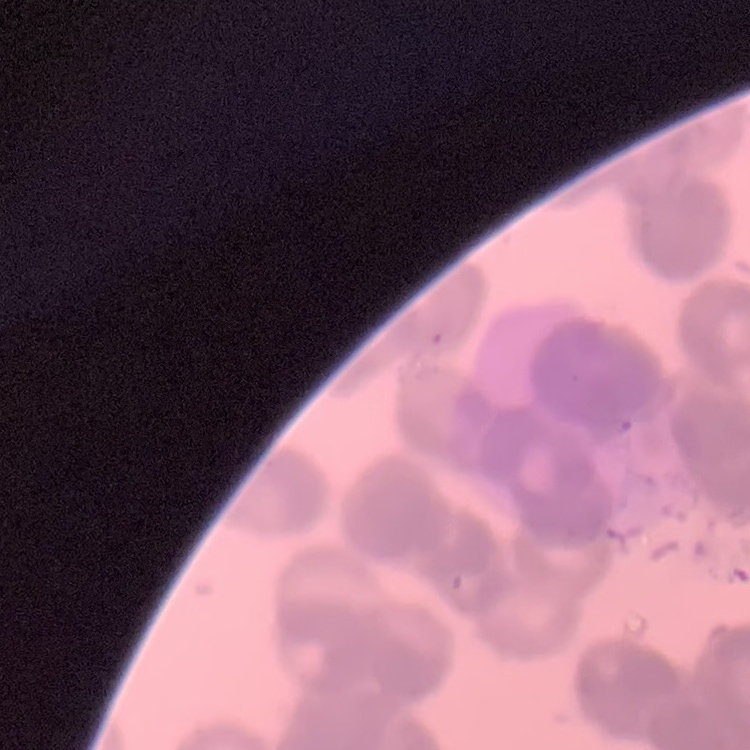
Summary:
  - Erythrocyte morphology: rouleaux formation
  - Image type: square crop of a larger photomicrograph
  - Stain: Field's or Giemsa
  - Preparation: thin peripheral smear